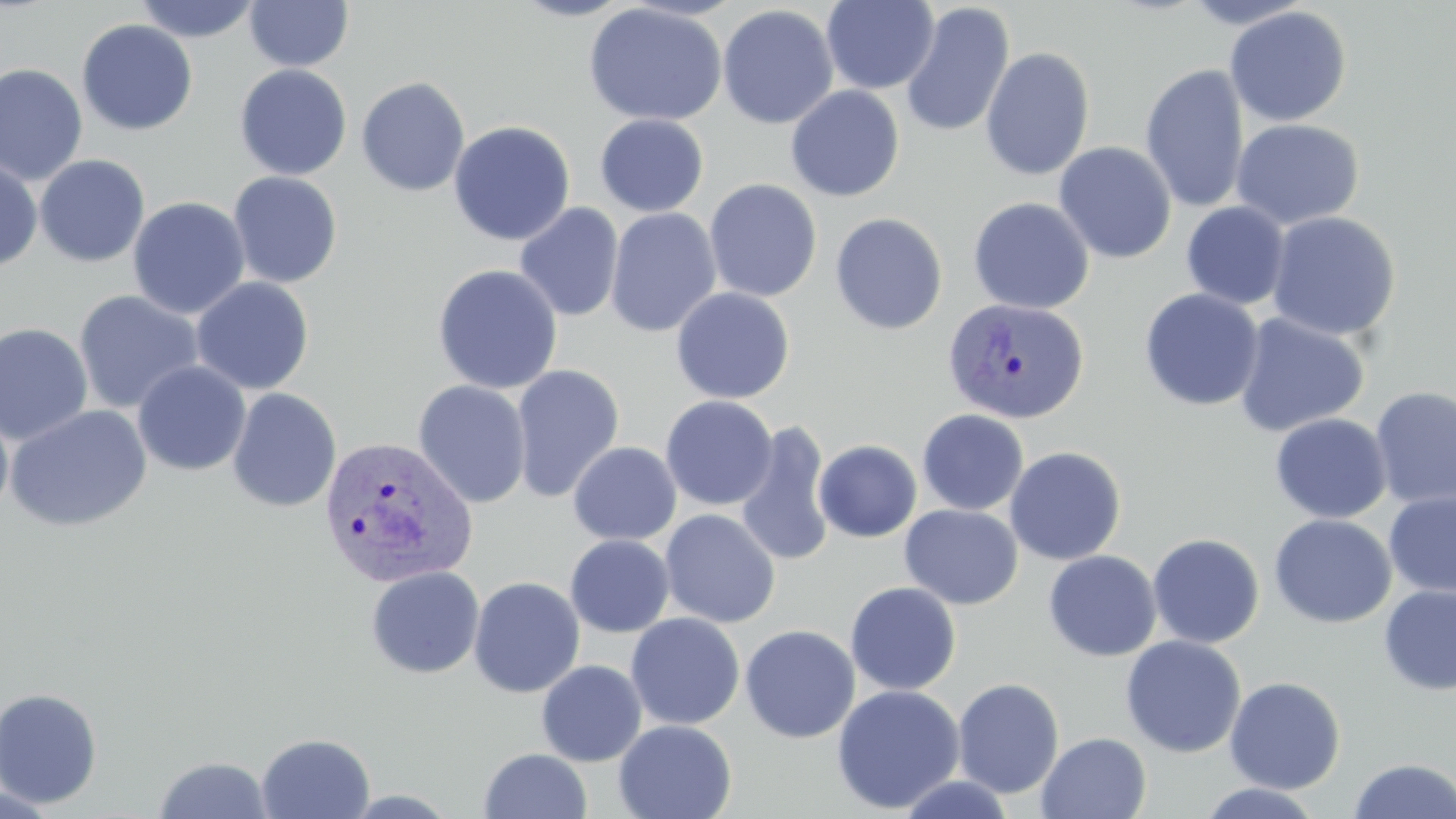 Approximate bounding boxes as named x1/y1/x2/y2 corners in pixels. Uninfected red blood cell locations: (x1=132, y1=0, x2=261, y2=43), (x1=244, y1=0, x2=354, y2=71), (x1=510, y1=0, x2=633, y2=22), (x1=821, y1=0, x2=940, y2=94), (x1=583, y1=2, x2=728, y2=126), (x1=900, y1=2, x2=1015, y2=138), (x1=717, y1=4, x2=839, y2=129), (x1=1224, y1=5, x2=1352, y2=127), (x1=76, y1=19, x2=198, y2=136), (x1=979, y1=47, x2=1095, y2=181), (x1=0, y1=62, x2=88, y2=186), (x1=1140, y1=63, x2=1249, y2=214), (x1=234, y1=64, x2=352, y2=180), (x1=356, y1=76, x2=470, y2=196), (x1=785, y1=85, x2=905, y2=202), (x1=595, y1=114, x2=709, y2=217), (x1=1231, y1=118, x2=1365, y2=230), (x1=448, y1=120, x2=576, y2=246), (x1=1053, y1=141, x2=1177, y2=263), (x1=34, y1=154, x2=150, y2=267), (x1=0, y1=157, x2=42, y2=273), (x1=227, y1=171, x2=343, y2=288), (x1=704, y1=178, x2=822, y2=302), (x1=128, y1=196, x2=250, y2=319), (x1=967, y1=197, x2=1095, y2=314), (x1=1181, y1=202, x2=1290, y2=310), (x1=514, y1=203, x2=624, y2=322), (x1=605, y1=207, x2=722, y2=337), (x1=1266, y1=211, x2=1401, y2=341), (x1=830, y1=212, x2=947, y2=335), (x1=432, y1=264, x2=563, y2=394), (x1=191, y1=277, x2=314, y2=395), (x1=671, y1=287, x2=795, y2=404), (x1=1139, y1=288, x2=1264, y2=411), (x1=73, y1=290, x2=205, y2=414), (x1=1233, y1=312, x2=1370, y2=437), (x1=0, y1=322, x2=94, y2=445), (x1=133, y1=360, x2=251, y2=476), (x1=510, y1=364, x2=625, y2=503), (x1=413, y1=379, x2=531, y2=508), (x1=1370, y1=385, x2=1456, y2=510), (x1=227, y1=388, x2=342, y2=512), (x1=660, y1=395, x2=778, y2=511), (x1=0, y1=404, x2=14, y2=525), (x1=4, y1=404, x2=152, y2=533), (x1=917, y1=409, x2=1029, y2=516), (x1=1269, y1=412, x2=1392, y2=523), (x1=733, y1=417, x2=834, y2=568), (x1=814, y1=440, x2=922, y2=543), (x1=568, y1=441, x2=682, y2=546), (x1=1004, y1=445, x2=1127, y2=565), (x1=1384, y1=491, x2=1456, y2=599), (x1=900, y1=504, x2=1023, y2=609), (x1=659, y1=509, x2=781, y2=628), (x1=1268, y1=514, x2=1396, y2=629), (x1=1147, y1=533, x2=1265, y2=648), (x1=565, y1=534, x2=674, y2=638), (x1=1043, y1=550, x2=1162, y2=662), (x1=365, y1=566, x2=485, y2=679), (x1=468, y1=576, x2=585, y2=698), (x1=845, y1=582, x2=962, y2=695), (x1=1377, y1=585, x2=1456, y2=696), (x1=626, y1=612, x2=746, y2=730), (x1=740, y1=624, x2=861, y2=743), (x1=1120, y1=635, x2=1246, y2=758), (x1=536, y1=659, x2=647, y2=766), (x1=1224, y1=676, x2=1346, y2=794), (x1=952, y1=677, x2=1065, y2=798), (x1=831, y1=684, x2=965, y2=814), (x1=0, y1=688, x2=102, y2=809), (x1=613, y1=720, x2=737, y2=819), (x1=1036, y1=731, x2=1152, y2=819), (x1=256, y1=732, x2=375, y2=818), (x1=478, y1=748, x2=593, y2=819), (x1=152, y1=755, x2=275, y2=818), (x1=1347, y1=758, x2=1456, y2=818), (x1=892, y1=773, x2=1017, y2=818), (x1=1195, y1=783, x2=1327, y2=818), (x1=0, y1=785, x2=60, y2=818). Plasmodium vivax-infected red blood cell locations: (x1=942, y1=297, x2=1089, y2=425), (x1=316, y1=435, x2=477, y2=589). Slide-level diagnosis: Plasmodium vivax. Single field of view. 1000x magnification. Image is 1456×819 pixels. Light microscopy. May-Grünwald-Giemsa stain. Thin blood smear.